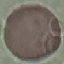
Result: negative for malaria parasites. Photographed with a smartphone camera at the microscope eyepiece. Giemsa-stained preparation. Cell patch, automatically extracted from a larger field of view and resized to 64 × 64 pixels. Thin blood film.